Identify the parasite.
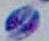

Toxoplasma gondii.

magnification = 1000x
modality = micrograph